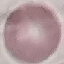
Result: no malaria parasites seen. Cell patch, automatically extracted from a larger field of view and resized to 64 × 64 pixels. Acquired by smartphone through the microscope eyepiece. Giemsa stain. Thin blood smear.